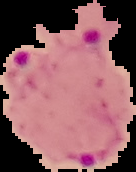

Summary:
  - Malaria status: parasitized
  - Preparation: thin blood smear
  - Image type: segmented cell region on a black background
  - Image size: 136×172 pixels